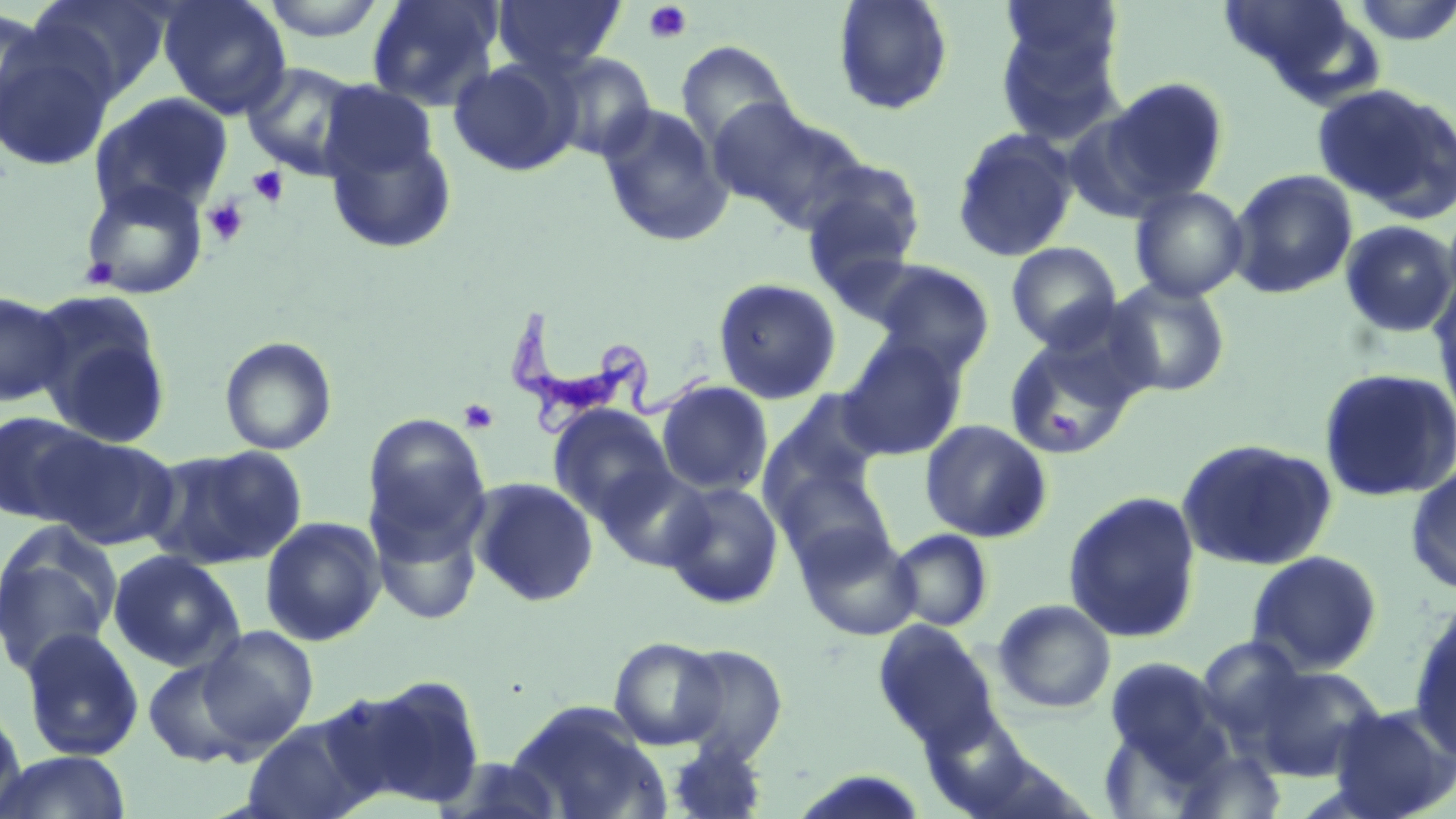
slide_level_diagnosis: Trypanosoma brucei
platelet_locations: 'approximate bounding boxes as named x1/y1/x2/y2 corners in pixels: (x1=642, y1=2, x2=692, y2=44), (x1=248, y1=166, x2=289, y2=208), (x1=202, y1=197, x2=249, y2=246), (x1=86, y1=258, x2=118, y2=288), (x1=459, y1=398, x2=499, y2=434)'
preparation: thin blood smear
magnification: 1000x
stain: May-Grünwald-Giemsa
field_of_view: one of a larger specimen
modality: optical microscopy
trypanosoma_brucei_locations: 'approximate bounding boxes as named x1/y1/x2/y2 corners in pixels: (x1=504, y1=306, x2=714, y2=440)'
uninfected_red_blood_cell_locations: 'approximate bounding boxes as named x1/y1/x2/y2 corners in pixels: (x1=25, y1=0, x2=173, y2=102), (x1=158, y1=0, x2=291, y2=119), (x1=257, y1=0, x2=392, y2=42), (x1=365, y1=0, x2=503, y2=111), (x1=491, y1=0, x2=625, y2=78), (x1=833, y1=0, x2=954, y2=116), (x1=1001, y1=0, x2=1123, y2=81), (x1=1, y1=7, x2=52, y2=138), (x1=994, y1=20, x2=1126, y2=148), (x1=0, y1=32, x2=116, y2=172), (x1=675, y1=40, x2=796, y2=154), (x1=546, y1=52, x2=656, y2=162), (x1=448, y1=57, x2=579, y2=176), (x1=240, y1=61, x2=366, y2=180), (x1=1101, y1=77, x2=1230, y2=206), (x1=319, y1=80, x2=439, y2=188), (x1=1312, y1=83, x2=1456, y2=218), (x1=89, y1=92, x2=233, y2=217), (x1=708, y1=98, x2=850, y2=228), (x1=598, y1=103, x2=732, y2=247), (x1=323, y1=123, x2=458, y2=255), (x1=951, y1=128, x2=1078, y2=263), (x1=799, y1=158, x2=927, y2=286), (x1=1228, y1=169, x2=1357, y2=299), (x1=79, y1=178, x2=209, y2=300), (x1=1129, y1=186, x2=1249, y2=303), (x1=1339, y1=220, x2=1456, y2=339), (x1=1005, y1=241, x2=1122, y2=351), (x1=868, y1=261, x2=995, y2=373), (x1=1430, y1=274, x2=1456, y2=421), (x1=712, y1=277, x2=843, y2=405), (x1=1105, y1=278, x2=1231, y2=398), (x1=0, y1=289, x2=72, y2=408), (x1=30, y1=294, x2=173, y2=448), (x1=1003, y1=333, x2=1139, y2=459), (x1=219, y1=336, x2=337, y2=455), (x1=837, y1=337, x2=968, y2=461), (x1=1317, y1=367, x2=1456, y2=502), (x1=656, y1=380, x2=773, y2=496), (x1=766, y1=388, x2=887, y2=502), (x1=548, y1=405, x2=675, y2=525), (x1=0, y1=410, x2=103, y2=526), (x1=361, y1=413, x2=491, y2=558), (x1=919, y1=419, x2=1052, y2=543), (x1=37, y1=431, x2=180, y2=551), (x1=1176, y1=438, x2=1337, y2=571), (x1=147, y1=445, x2=307, y2=572), (x1=1405, y1=464, x2=1456, y2=594), (x1=597, y1=466, x2=715, y2=571), (x1=773, y1=466, x2=894, y2=571), (x1=470, y1=478, x2=598, y2=607), (x1=661, y1=481, x2=784, y2=609), (x1=1062, y1=491, x2=1202, y2=643), (x1=368, y1=504, x2=484, y2=626), (x1=260, y1=517, x2=385, y2=646), (x1=0, y1=523, x2=122, y2=678), (x1=796, y1=524, x2=920, y2=640), (x1=889, y1=529, x2=993, y2=631), (x1=108, y1=550, x2=244, y2=672), (x1=1245, y1=550, x2=1384, y2=676), (x1=993, y1=599, x2=1116, y2=714), (x1=1408, y1=602, x2=1456, y2=761), (x1=874, y1=621, x2=999, y2=751), (x1=196, y1=625, x2=319, y2=751), (x1=18, y1=626, x2=145, y2=762), (x1=1196, y1=635, x2=1308, y2=737), (x1=609, y1=636, x2=728, y2=751), (x1=671, y1=643, x2=789, y2=763), (x1=1103, y1=656, x2=1228, y2=775), (x1=143, y1=657, x2=255, y2=767), (x1=1251, y1=663, x2=1386, y2=781), (x1=335, y1=675, x2=488, y2=811), (x1=0, y1=700, x2=27, y2=818), (x1=508, y1=702, x2=668, y2=819), (x1=1327, y1=703, x2=1456, y2=819), (x1=242, y1=715, x2=377, y2=819), (x1=665, y1=739, x2=768, y2=818), (x1=1169, y1=748, x2=1289, y2=819), (x1=0, y1=750, x2=132, y2=818), (x1=436, y1=756, x2=568, y2=818)'
image_size: 1456×819 pixels